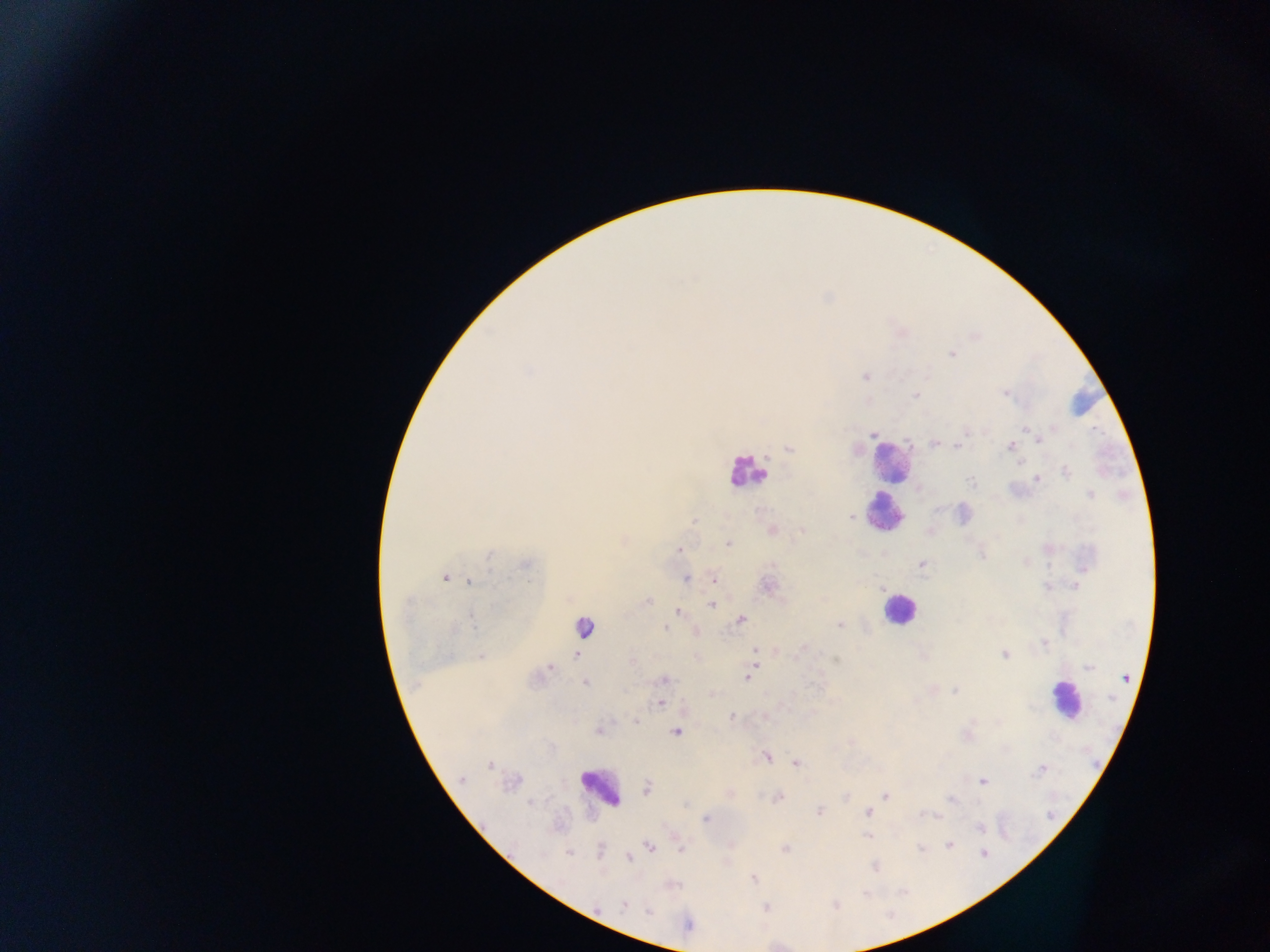
malaria_parasite_locations: 'approximate centers as x y in pixels: 952 354; 528 371; 865 377; 1005 394; 915 396; 1053 428; 1025 430; 964 432; 873 434; 1034 434; 1039 439; 933 443; 958 445; 1011 446; 789 449; 1067 472; 1038 479; 971 482; 1091 495; 850 517; 694 521; 772 531; 802 531; 728 544; 679 550; 982 555; 489 557; 526 564; 921 564; 445 578; 686 578; 714 579; 469 582; 767 586; 1077 586; 1047 587; 881 589; 647 601; 712 605; 678 611; 742 620; 473 621; 840 625; 666 629; 1043 643; 755 650; 1005 654; 576 655; 481 656; 836 660; 632 663; 1088 667; 549 668; 749 677; 1126 677; 662 679; 585 683; 954 691; 661 703; 732 716; 636 721; 598 731; 676 732; 766 756; 796 763; 490 765; 1042 770; 461 779; 983 781; 648 787; 886 795; 778 797; 950 800; 531 803; 869 811; 820 812; 935 816; 706 819; 980 828; 866 837; 950 845; 649 847; 921 848; 681 849; 785 849; 569 853; 983 853; 630 858; 875 866; 753 878; 624 904; 835 905; 766 907; 649 911; 688 925'
field_of_view: single
country: Ghana
preparation: thick blood film
capture: mobile-phone photograph through a microscope
image_size: 1270×952 pixels
leukocyte_locations: 'approximate centers as x y in pixels: 891 461; 746 471; 886 513; 899 608; 584 622; 1064 699; 601 786'